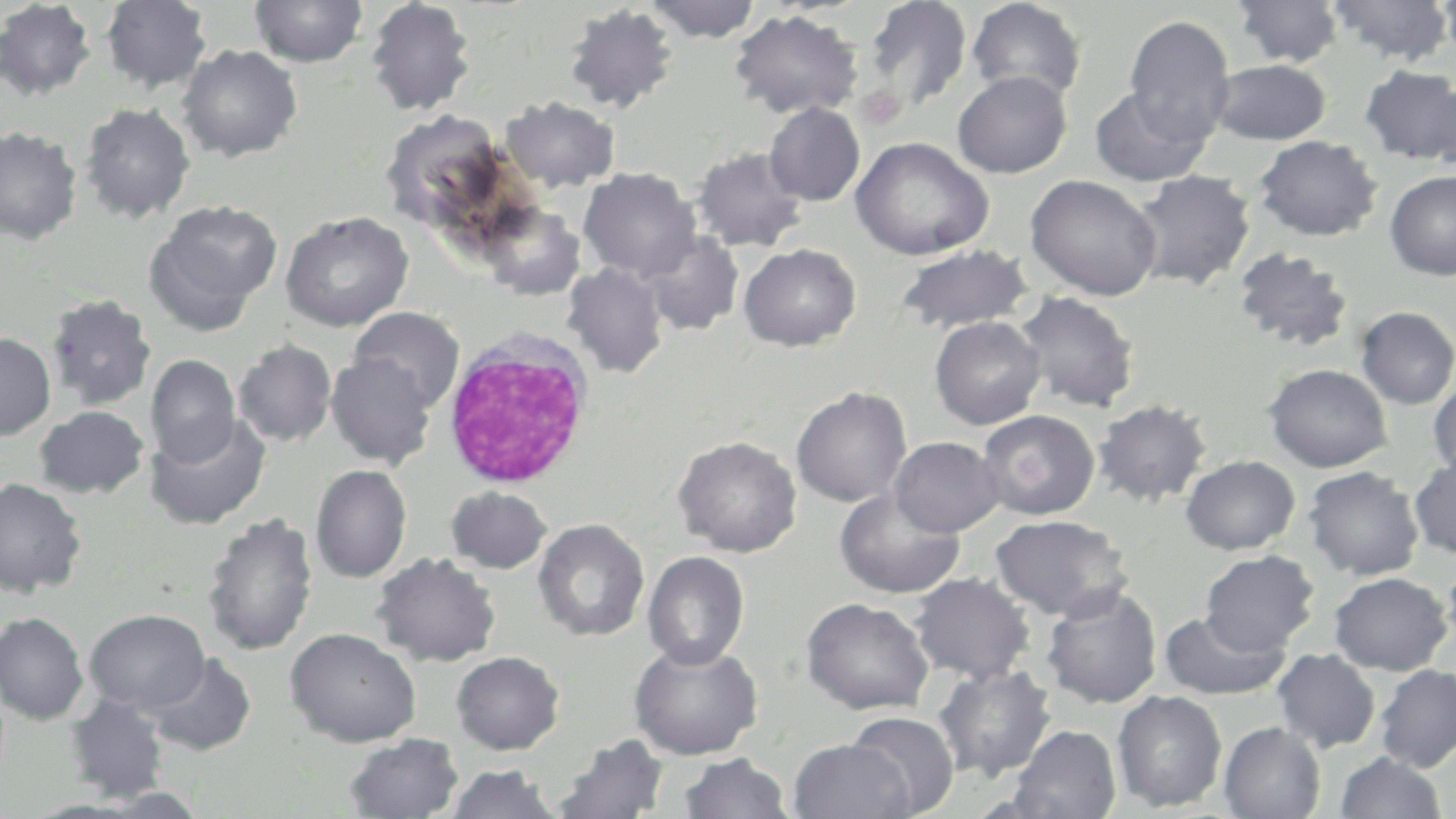
Approximate bounding boxes as (x1, y1, x2, y2) in pixels. White blood cell locations: (442, 326, 595, 490). Uninfected red blood cell locations: (101, 0, 212, 92), (250, 0, 368, 67), (365, 0, 477, 116), (644, 0, 762, 42), (862, 0, 972, 113), (965, 0, 1088, 103), (1232, 0, 1346, 67), (1326, 0, 1455, 65), (1436, 0, 1456, 63), (0, 1, 97, 100), (563, 4, 680, 114), (729, 9, 863, 119), (1124, 15, 1235, 146), (177, 44, 302, 161), (1210, 59, 1331, 144), (1359, 65, 1456, 165), (952, 71, 1072, 178), (1425, 79, 1456, 175), (1089, 87, 1211, 187), (499, 96, 620, 193), (80, 102, 195, 223), (764, 102, 865, 206), (0, 126, 82, 245), (1253, 135, 1382, 241), (850, 136, 994, 261), (691, 146, 808, 252), (578, 167, 701, 280), (1131, 169, 1255, 289), (1385, 170, 1456, 280), (1025, 173, 1163, 301), (147, 200, 283, 326), (479, 201, 586, 300), (280, 211, 414, 332), (639, 230, 744, 336), (738, 243, 861, 351), (895, 244, 1033, 333), (1232, 247, 1355, 352), (562, 263, 670, 378), (1015, 291, 1140, 413), (46, 293, 156, 411), (1355, 306, 1456, 409), (349, 307, 465, 412), (929, 315, 1046, 430), (0, 332, 56, 439), (233, 340, 336, 446), (325, 353, 437, 468), (145, 354, 240, 466), (1263, 363, 1392, 472), (1427, 378, 1456, 480), (791, 386, 912, 507), (1092, 400, 1211, 506), (35, 405, 149, 497), (977, 409, 1099, 520), (146, 413, 270, 530), (674, 435, 802, 557), (889, 436, 1005, 537), (1180, 455, 1300, 554), (1409, 455, 1456, 560), (311, 464, 411, 583), (1303, 465, 1424, 580), (0, 478, 87, 598), (446, 486, 552, 573), (833, 488, 965, 600), (202, 512, 319, 657), (990, 514, 1132, 620), (533, 518, 650, 641), (1199, 550, 1319, 655), (642, 551, 750, 669), (371, 552, 501, 667), (1441, 555, 1456, 654), (909, 572, 1035, 683), (1329, 572, 1453, 675), (1358, 572, 1456, 772), (1040, 585, 1162, 709), (801, 597, 934, 715), (84, 608, 210, 714), (1158, 609, 1292, 701), (0, 612, 88, 725), (285, 627, 421, 746), (628, 641, 763, 760), (1271, 648, 1381, 753), (451, 651, 565, 754), (146, 652, 256, 756), (933, 663, 1056, 782), (1375, 664, 1456, 773), (1112, 689, 1228, 812), (66, 694, 170, 802), (846, 711, 959, 816), (1219, 722, 1326, 819), (1007, 725, 1121, 819), (343, 733, 465, 819), (552, 734, 670, 818), (788, 738, 914, 819), (1334, 751, 1448, 818), (679, 752, 793, 819), (443, 763, 563, 819), (95, 787, 209, 818). Platelet locations: (855, 85, 905, 130). Slide-level diagnosis: negative for blood parasites. Image is 1456×819 pixels. May-Grünwald-Giemsa-stained preparation. Thin blood film. Optical microscopy. Single field of view. Captured at 1000x magnification.